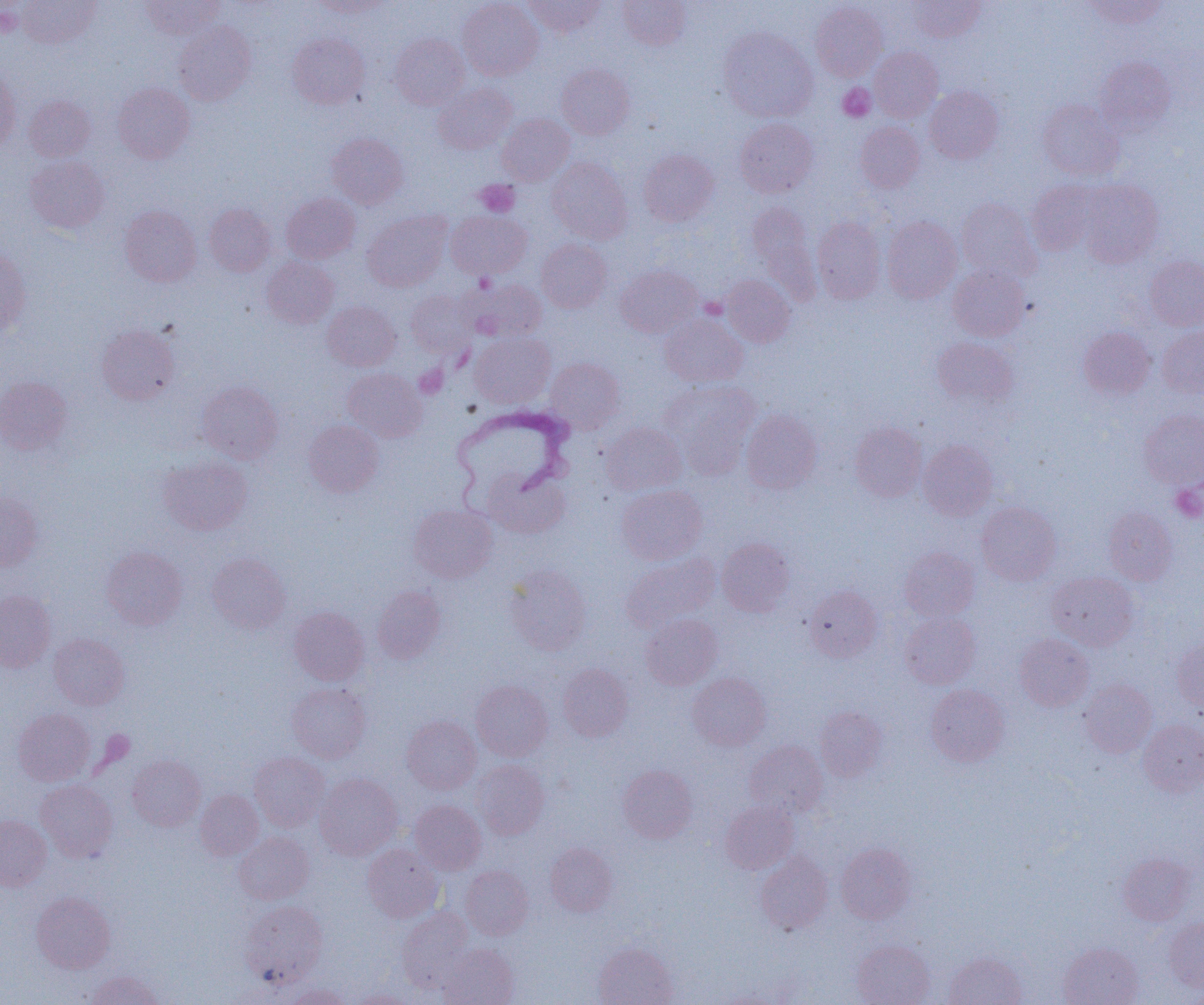
{
  "trypanosoma_brucei_locations": "approximate bounding boxes as named x1/y1/x2/y2 corners in pixels: (x1=450, y1=405, x2=575, y2=507)",
  "slide_level_diagnosis": "Trypanosoma brucei",
  "field_of_view": "one of a larger specimen",
  "magnification": "1000x",
  "image_size": "1204×1005 pixels",
  "uninfected_red_blood_cell_locations": "approximate bounding boxes as named x1/y1/x2/y2 corners in pixels: (x1=18, y1=0, x2=99, y2=47), (x1=140, y1=0, x2=225, y2=39), (x1=310, y1=0, x2=392, y2=17), (x1=457, y1=0, x2=543, y2=80), (x1=524, y1=0, x2=606, y2=37), (x1=618, y1=0, x2=689, y2=50), (x1=908, y1=0, x2=985, y2=41), (x1=1085, y1=0, x2=1169, y2=29), (x1=810, y1=2, x2=887, y2=81), (x1=174, y1=21, x2=256, y2=106), (x1=718, y1=27, x2=818, y2=122), (x1=288, y1=32, x2=369, y2=108), (x1=390, y1=34, x2=469, y2=109), (x1=870, y1=46, x2=943, y2=121), (x1=1095, y1=57, x2=1176, y2=134), (x1=556, y1=64, x2=635, y2=139), (x1=0, y1=67, x2=20, y2=152), (x1=112, y1=82, x2=195, y2=163), (x1=433, y1=82, x2=517, y2=154), (x1=924, y1=86, x2=1003, y2=163), (x1=24, y1=95, x2=96, y2=161), (x1=1038, y1=99, x2=1123, y2=181), (x1=497, y1=113, x2=574, y2=186), (x1=734, y1=118, x2=817, y2=197), (x1=855, y1=121, x2=925, y2=193), (x1=327, y1=133, x2=408, y2=209), (x1=638, y1=149, x2=719, y2=226), (x1=24, y1=156, x2=109, y2=233), (x1=547, y1=157, x2=633, y2=244), (x1=1078, y1=179, x2=1164, y2=267), (x1=1026, y1=180, x2=1101, y2=256), (x1=281, y1=193, x2=360, y2=263), (x1=956, y1=197, x2=1042, y2=281), (x1=747, y1=202, x2=816, y2=288), (x1=204, y1=203, x2=275, y2=276), (x1=120, y1=205, x2=201, y2=286), (x1=445, y1=210, x2=531, y2=280), (x1=362, y1=212, x2=451, y2=292), (x1=812, y1=216, x2=885, y2=304), (x1=881, y1=216, x2=962, y2=303), (x1=536, y1=239, x2=611, y2=312), (x1=0, y1=249, x2=31, y2=335), (x1=1145, y1=255, x2=1204, y2=331), (x1=261, y1=256, x2=338, y2=328), (x1=616, y1=265, x2=702, y2=337), (x1=948, y1=265, x2=1029, y2=341), (x1=720, y1=275, x2=796, y2=347), (x1=460, y1=278, x2=546, y2=343), (x1=406, y1=290, x2=476, y2=357), (x1=322, y1=301, x2=400, y2=371), (x1=660, y1=314, x2=748, y2=388), (x1=96, y1=323, x2=180, y2=405), (x1=1078, y1=326, x2=1156, y2=399), (x1=1157, y1=326, x2=1204, y2=398), (x1=470, y1=333, x2=555, y2=408), (x1=932, y1=337, x2=1018, y2=408), (x1=545, y1=358, x2=625, y2=431), (x1=342, y1=368, x2=427, y2=442), (x1=0, y1=376, x2=72, y2=454), (x1=661, y1=379, x2=760, y2=474), (x1=197, y1=381, x2=283, y2=463), (x1=1139, y1=409, x2=1204, y2=490), (x1=741, y1=410, x2=822, y2=494), (x1=303, y1=420, x2=383, y2=497), (x1=601, y1=422, x2=687, y2=496), (x1=850, y1=423, x2=927, y2=501), (x1=918, y1=440, x2=997, y2=520), (x1=158, y1=455, x2=252, y2=535), (x1=483, y1=468, x2=571, y2=539), (x1=617, y1=485, x2=707, y2=565), (x1=0, y1=492, x2=44, y2=571), (x1=976, y1=502, x2=1062, y2=585), (x1=408, y1=503, x2=498, y2=583), (x1=1104, y1=507, x2=1177, y2=585), (x1=716, y1=537, x2=795, y2=616), (x1=101, y1=546, x2=188, y2=630), (x1=899, y1=547, x2=980, y2=622), (x1=207, y1=553, x2=291, y2=633), (x1=621, y1=553, x2=719, y2=632), (x1=504, y1=564, x2=592, y2=655), (x1=1047, y1=571, x2=1139, y2=651), (x1=372, y1=586, x2=446, y2=664), (x1=805, y1=586, x2=882, y2=662), (x1=0, y1=590, x2=56, y2=672), (x1=289, y1=606, x2=369, y2=685), (x1=900, y1=612, x2=980, y2=688), (x1=641, y1=614, x2=722, y2=690), (x1=49, y1=633, x2=129, y2=710), (x1=1015, y1=634, x2=1093, y2=711), (x1=1172, y1=639, x2=1204, y2=714), (x1=558, y1=664, x2=633, y2=741), (x1=687, y1=672, x2=771, y2=751), (x1=1079, y1=679, x2=1157, y2=757), (x1=471, y1=680, x2=552, y2=761), (x1=286, y1=682, x2=371, y2=763), (x1=926, y1=684, x2=1009, y2=766), (x1=815, y1=706, x2=888, y2=781), (x1=14, y1=708, x2=95, y2=786), (x1=402, y1=715, x2=481, y2=794), (x1=1138, y1=719, x2=1204, y2=796), (x1=744, y1=740, x2=828, y2=816), (x1=249, y1=752, x2=329, y2=831), (x1=127, y1=755, x2=205, y2=831), (x1=472, y1=759, x2=549, y2=839), (x1=618, y1=765, x2=698, y2=843), (x1=314, y1=773, x2=403, y2=860), (x1=35, y1=780, x2=118, y2=862), (x1=196, y1=789, x2=264, y2=860), (x1=410, y1=800, x2=486, y2=875), (x1=720, y1=801, x2=799, y2=874), (x1=0, y1=816, x2=51, y2=890), (x1=234, y1=832, x2=314, y2=904), (x1=545, y1=842, x2=617, y2=916), (x1=836, y1=843, x2=916, y2=924), (x1=362, y1=844, x2=443, y2=923), (x1=755, y1=852, x2=833, y2=934), (x1=1118, y1=852, x2=1194, y2=925), (x1=460, y1=865, x2=533, y2=940), (x1=32, y1=892, x2=115, y2=973), (x1=240, y1=900, x2=328, y2=987), (x1=397, y1=907, x2=474, y2=991), (x1=1165, y1=917, x2=1204, y2=992), (x1=852, y1=940, x2=935, y2=1005), (x1=593, y1=942, x2=678, y2=1005), (x1=1060, y1=942, x2=1143, y2=1005), (x1=438, y1=943, x2=519, y2=1005), (x1=944, y1=952, x2=1027, y2=1005), (x1=86, y1=970, x2=163, y2=1005), (x1=285, y1=983, x2=351, y2=1005), (x1=349, y1=989, x2=415, y2=1004)",
  "platelet_locations": "approximate bounding boxes as named x1/y1/x2/y2 corners in pixels: (x1=0, y1=6, x2=22, y2=38), (x1=838, y1=83, x2=875, y2=122), (x1=474, y1=180, x2=519, y2=217), (x1=1171, y1=484, x2=1204, y2=522)",
  "preparation": "thin blood smear",
  "modality": "light microscopy"
}